Locate leukocytes (white blood cells).
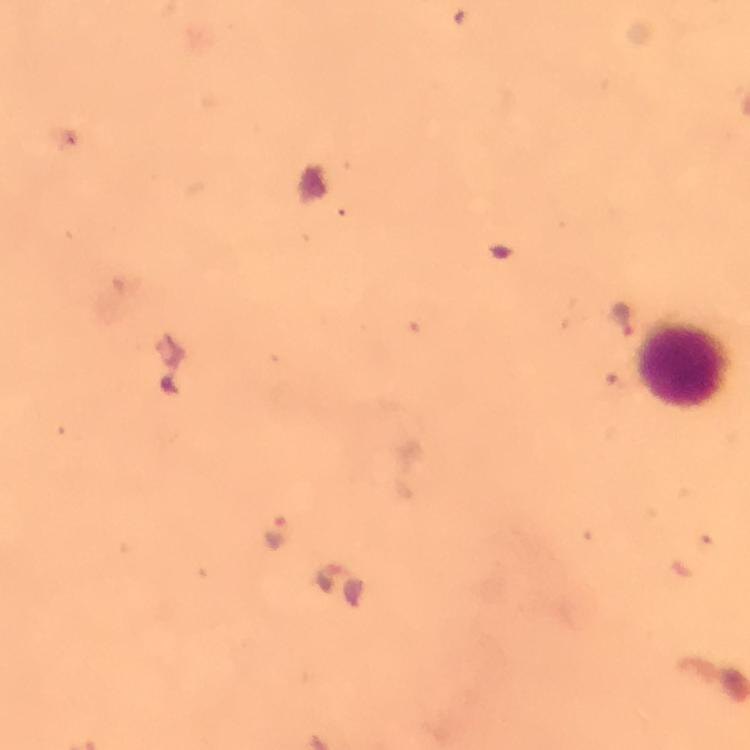
Approximate object centers, in pixels from the top-left corner.
Leukocytes: (x=686, y=367).

magnification = 100x
image size = 750×750 pixels
Plasmodium parasite locations = approximate object centers, in pixels from the top-left corner: (x=623, y=317), (x=273, y=532)
preparation = thick smear
capture = smartphone mounted on the microscope
context = from a diagnostic examination for malaria
immersion oil = used
cropped from = a single field of view
stain = Giemsa